Locate every leukocyte (white blood cell).
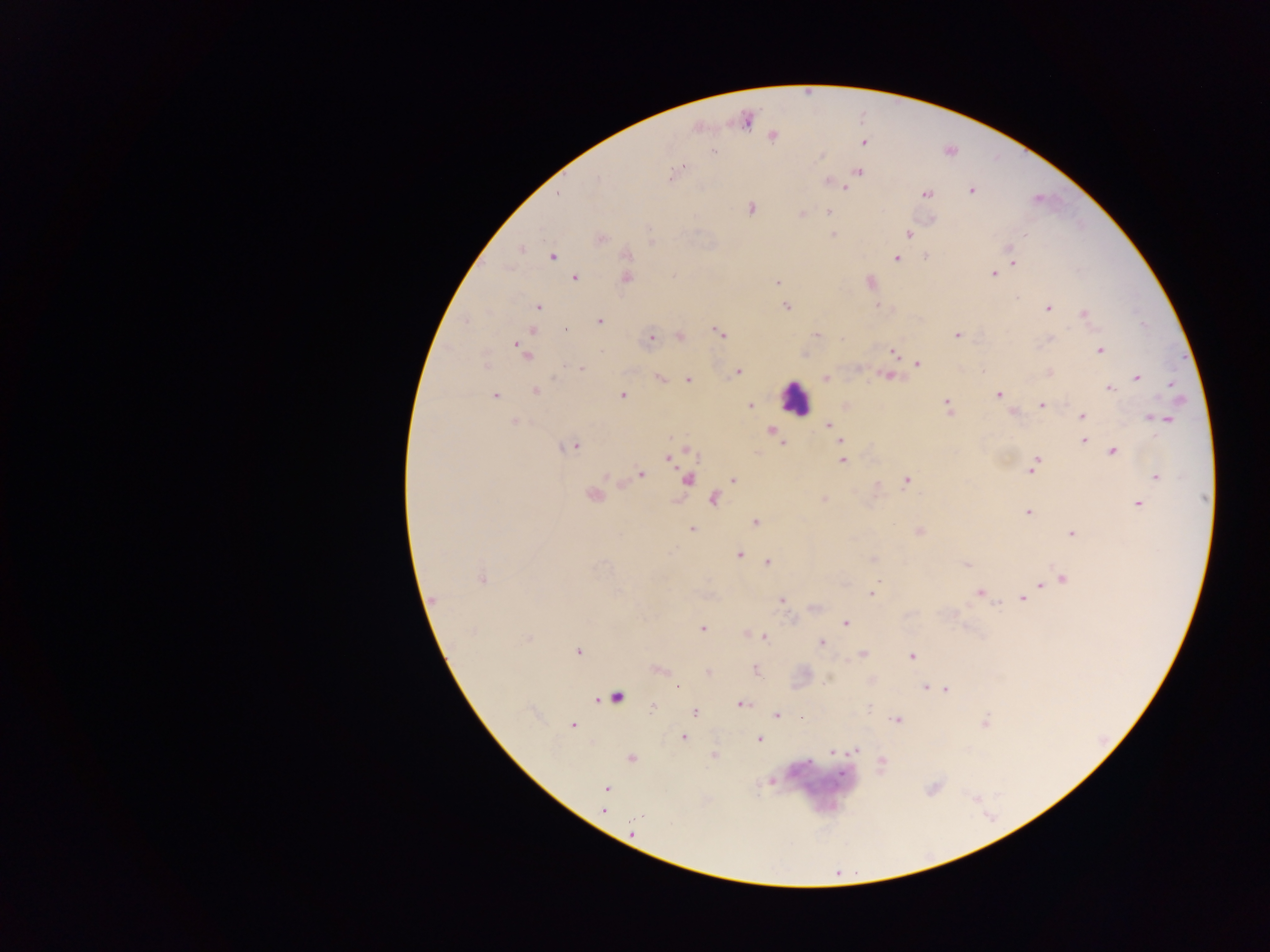
Approximate centers as {x, y} in pixels.
Leukocytes: {795, 398}.

Summary:
  - Plasmodium parasite locations: {746, 120}, {772, 137}, {863, 143}, {713, 151}, {682, 167}, {859, 172}, {674, 173}, {829, 182}, {846, 187}, {971, 190}, {559, 194}, {927, 194}, {750, 209}, {828, 212}, {802, 214}, {909, 234}, {833, 235}, {600, 238}, {652, 241}, {521, 249}, {1010, 253}, {627, 255}, {552, 256}, {926, 256}, {896, 258}, {1013, 261}, {993, 273}, {575, 278}, {626, 278}, {869, 281}, {777, 283}, {786, 306}, {537, 308}, {1048, 308}, {1083, 314}, {600, 321}, {565, 331}, {533, 332}, {719, 333}, {816, 334}, {956, 335}, {680, 336}, {651, 340}, {520, 347}, {1099, 350}, {892, 352}, {526, 353}, {486, 364}, {917, 364}, {580, 368}, {982, 371}, {738, 372}, {1049, 373}, {887, 376}, {825, 378}, {1137, 378}, {660, 379}, {688, 380}, {1171, 383}, {1110, 388}, {535, 391}, {494, 395}, {998, 395}, {622, 396}, {750, 405}, {1041, 405}, {947, 407}, {1013, 411}, {1082, 415}, {1153, 417}, {1162, 419}, {514, 421}, {829, 425}, {771, 431}, {775, 436}, {841, 441}, {1084, 441}, {783, 443}, {572, 446}, {1113, 451}, {691, 453}, {670, 457}, {842, 461}, {1032, 466}, {641, 474}, {606, 476}, {1156, 476}, {733, 479}, {687, 480}, {906, 481}, {591, 496}, {713, 500}, {824, 500}, {1139, 503}, {1028, 512}, {755, 523}, {692, 530}, {919, 531}, {1073, 533}, {739, 555}, {873, 559}, {768, 562}, {966, 565}, {481, 579}, {1063, 579}, {1040, 585}, {871, 593}, {979, 593}, {1023, 598}, {434, 600}, {782, 600}, {997, 604}, {846, 623}, {701, 628}, {471, 632}, {765, 637}, {528, 638}, {821, 643}, {577, 652}, {863, 654}, {912, 656}, {660, 670}, {756, 670}, {708, 673}, {673, 686}, {925, 687}, {677, 688}, {946, 690}, {616, 697}, {742, 704}, {653, 707}, {696, 713}, {777, 715}, {896, 720}, {572, 725}, {684, 738}, {759, 739}, {855, 751}, {833, 752}, {714, 755}, {631, 759}, {882, 762}, {773, 781}, {606, 788}, {604, 811}, {633, 832}
  - Field of view: single
  - Country: Ghana
  - Capture: mobile-phone photograph through a microscope
  - Preparation: thick blood smear
  - Image size: 1270×952 pixels